Assess this cell for malaria.
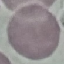
Uninfected.

Summary:
  - Stain: Giemsa
  - Preparation: thin blood smear
  - Capture: smartphone through the microscope eyepiece
  - Image type: automatically extracted cell patch, resized to 64 × 64 pixels